Outline every malaria parasite.
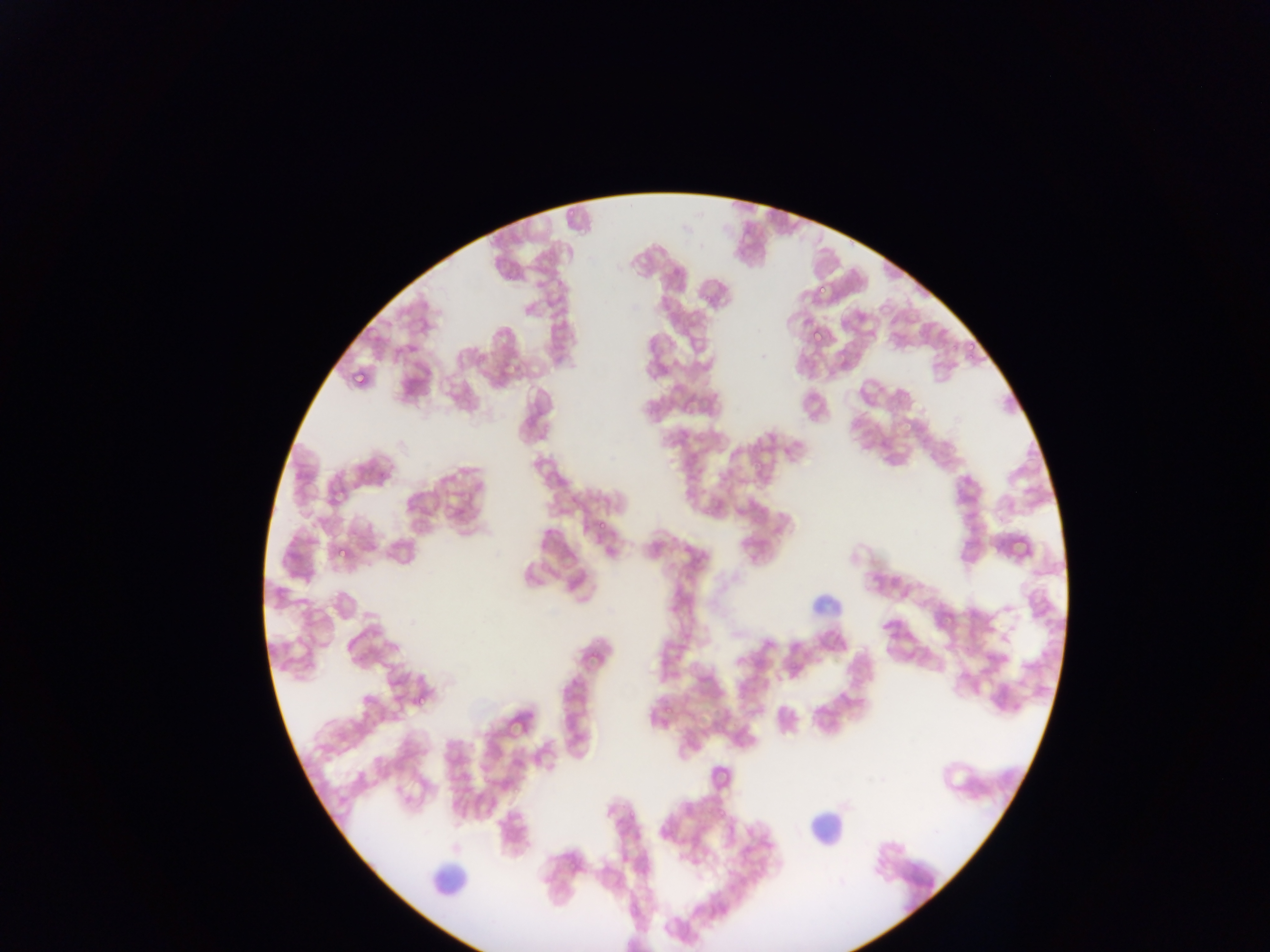

Approximate bounding boxes as {left, top, right, bottom} in pixels.
Malaria parasites: {814, 283, 827, 297}, {703, 291, 717, 304}, {803, 317, 815, 330}, {809, 327, 824, 342}, {835, 355, 852, 372}, {350, 367, 367, 386}, {904, 420, 919, 435}, {458, 489, 473, 506}, {711, 497, 725, 511}, {593, 520, 605, 532}, {335, 543, 350, 560}, {411, 693, 427, 709}, {654, 701, 667, 715}, {659, 702, 671, 714}.

{
  "capture": "mobile-phone photograph through a microscope",
  "preparation": "thin blood film",
  "field_of_view": "single",
  "leukocyte_locations": "approximate bounding boxes as {left, top, right, bottom} in pixels: {795, 587, 861, 620}, {789, 813, 855, 854}, {415, 853, 473, 901}",
  "image_size": "1270×952 pixels",
  "country": "Ghana"
}